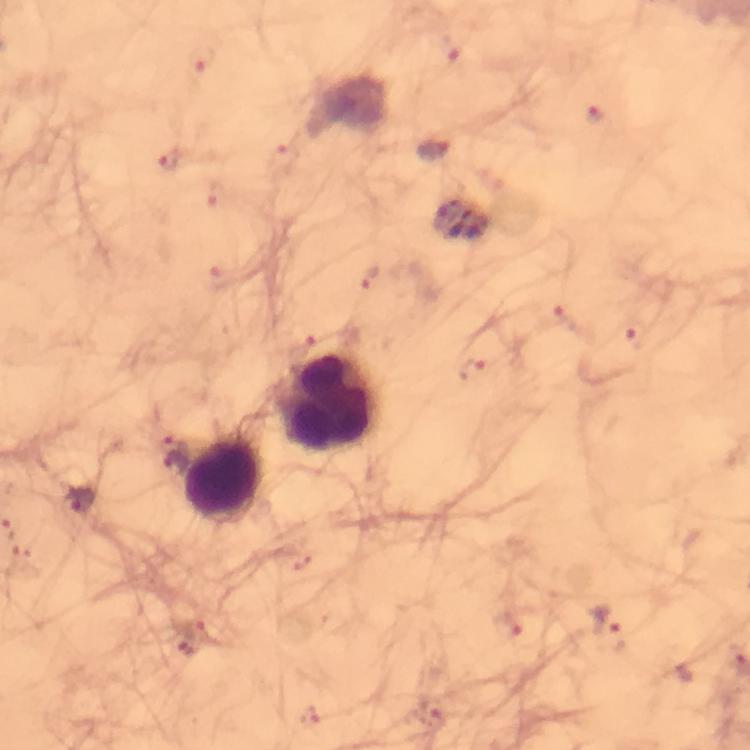
{
  "plasmodium_parasite_locations": "approximate centers as (x, y) in pixels: (435, 151), (79, 501), (604, 622)",
  "leukocyte_locations": "approximate centers as (x, y) in pixels: (330, 403), (226, 477)",
  "preparation": "thick smear",
  "context": "from a diagnostic examination for malaria",
  "stain": "Giemsa",
  "image_size": "750×750 pixels",
  "cropped_from": "a single field of view",
  "capture": "smartphone mounted on the microscope",
  "immersion_oil": "applied",
  "magnification": "100x"
}